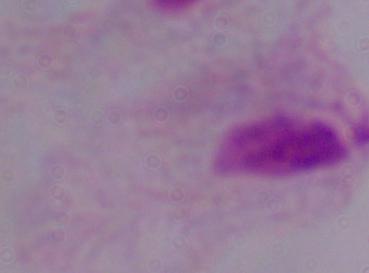
{
  "modality": "photomicrograph",
  "identification": "trichomonad",
  "magnification": "1000x"
}